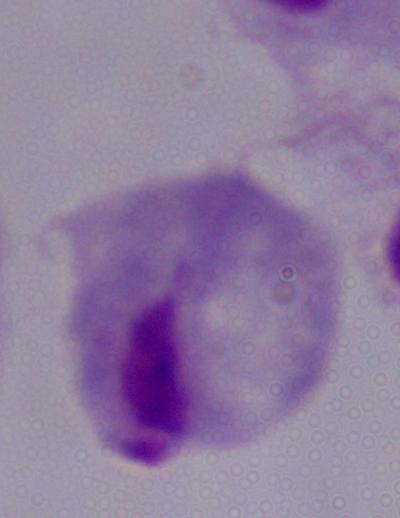

A trichomonad is shown. Photomicrograph. 1000x magnification.